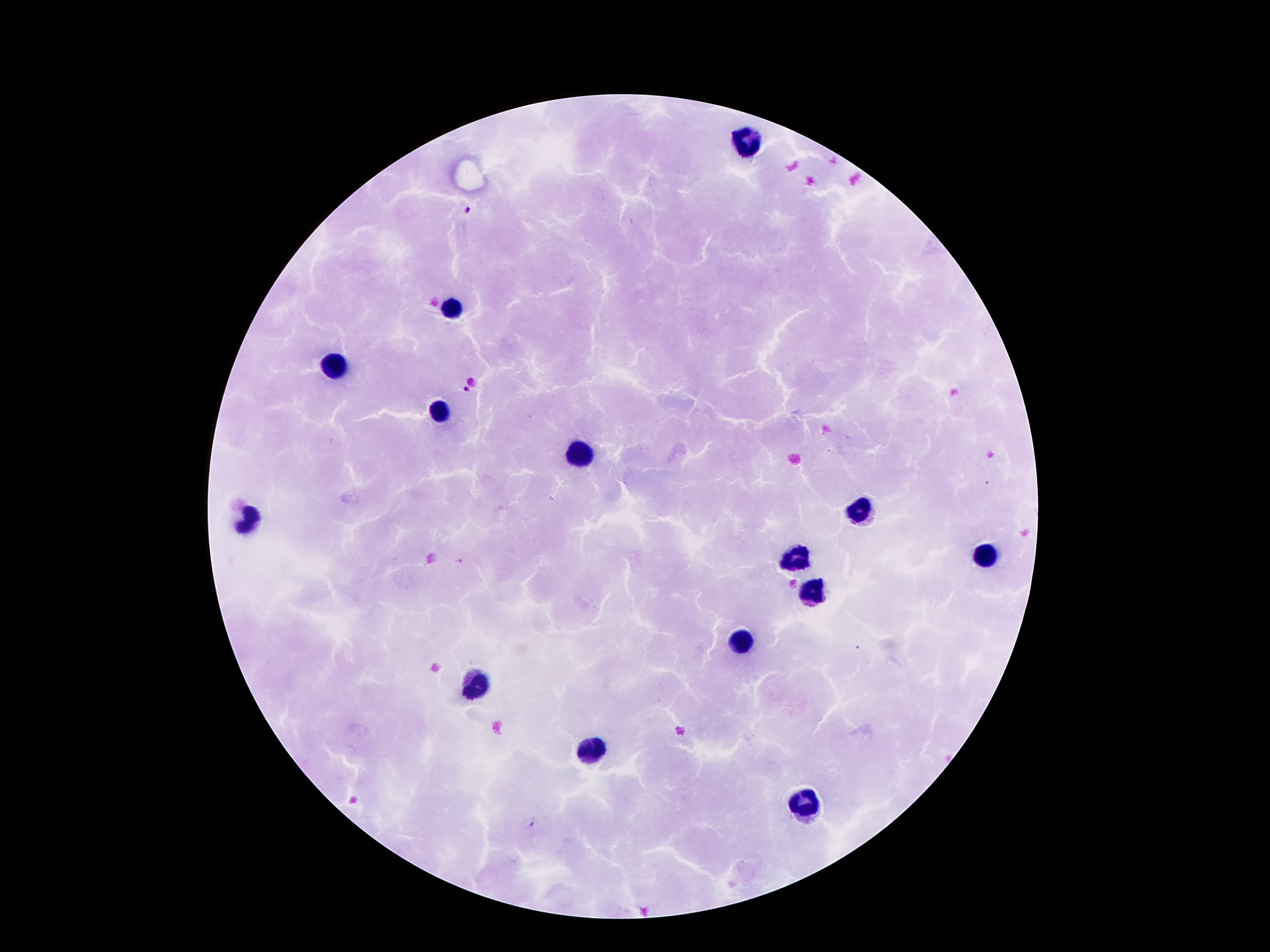
coordinate format = approximate centers as [x, y] in pixels
leukocyte locations = [746, 138], [450, 308], [339, 367], [441, 410], [578, 453], [859, 508], [248, 519], [984, 555], [793, 560], [814, 592], [737, 642], [477, 684], [590, 754], [800, 800]
malaria parasite locations = [467, 212], [464, 388], [459, 561], [531, 824]
patient malaria status = positive for Plasmodium falciparum
image size = 1270×952 pixels
preparation = thick blood film
stain = Giemsa
magnification = 100x
field of view = single
capture = smartphone through the microscope eyepiece